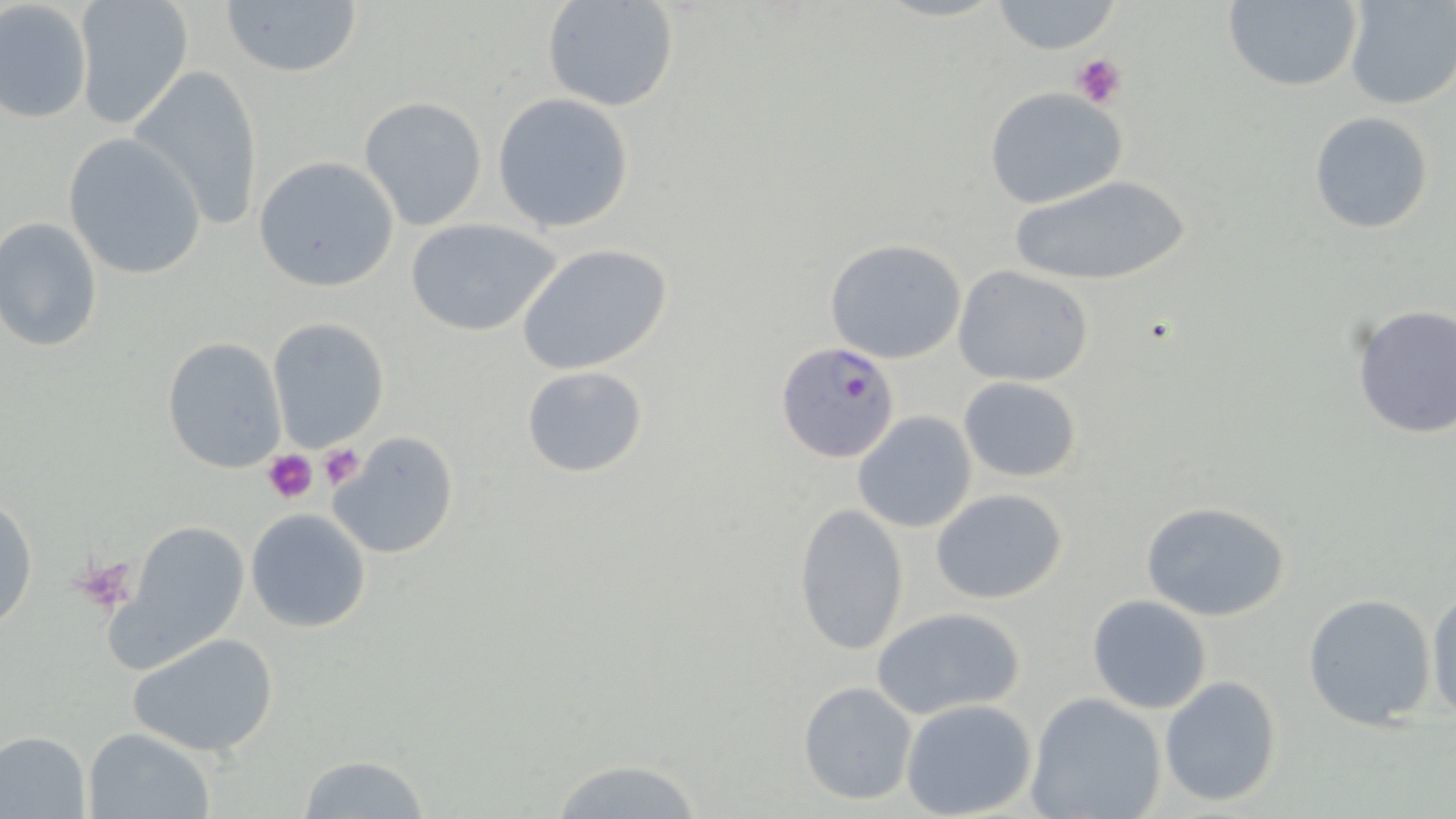

Summary:
  - Coordinate format: approximate bounding boxes as (x1, y1, x2, y2) in pixels
  - Uninfected red blood cell locations: (72, 0, 193, 131), (219, 0, 366, 78), (540, 0, 679, 113), (1221, 0, 1364, 91), (1343, 0, 1456, 110), (0, 2, 93, 124), (990, 2, 1121, 54), (129, 63, 265, 229), (982, 86, 1130, 211), (493, 92, 634, 234), (359, 95, 487, 230), (1309, 112, 1435, 233), (63, 134, 206, 280), (253, 156, 400, 293), (1004, 174, 1196, 288), (0, 216, 103, 352), (402, 216, 562, 337), (825, 239, 966, 363), (516, 243, 673, 377), (953, 266, 1096, 388), (1350, 303, 1456, 440), (266, 318, 390, 450), (162, 337, 286, 473), (521, 365, 650, 479), (958, 376, 1081, 483), (853, 411, 977, 533), (329, 432, 459, 560), (932, 490, 1069, 605), (0, 496, 38, 635), (1139, 500, 1290, 622), (792, 504, 908, 658), (246, 508, 372, 633), (102, 517, 252, 679), (1426, 585, 1456, 725), (1302, 593, 1438, 730), (1087, 594, 1213, 714), (872, 605, 1028, 718), (128, 632, 280, 758), (1159, 674, 1283, 807), (798, 681, 918, 805), (1025, 692, 1167, 819), (900, 698, 1037, 818), (83, 727, 219, 819), (0, 730, 91, 817), (298, 754, 431, 819), (547, 757, 712, 818)
  - Platelet locations: (1071, 51, 1127, 110), (317, 444, 367, 491), (263, 451, 317, 504), (72, 555, 137, 613)
  - Plasmodium falciparum-infected red blood cell locations: (776, 341, 903, 465)
  - Slide-level diagnosis: Plasmodium falciparum
  - Stain: May-Grünwald-Giemsa
  - Magnification: 1000x
  - Modality: optical microscopy
  - Preparation: thin blood smear
  - Image size: 1456×819 pixels
  - Field of view: one of a larger specimen